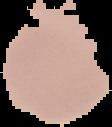
From a thin blood smear. Image is 112×127 pixels. Result: no Plasmodium parasites detected. The area outside the segmented cell region is set to black.